Locate every blood parasite and identify its species.
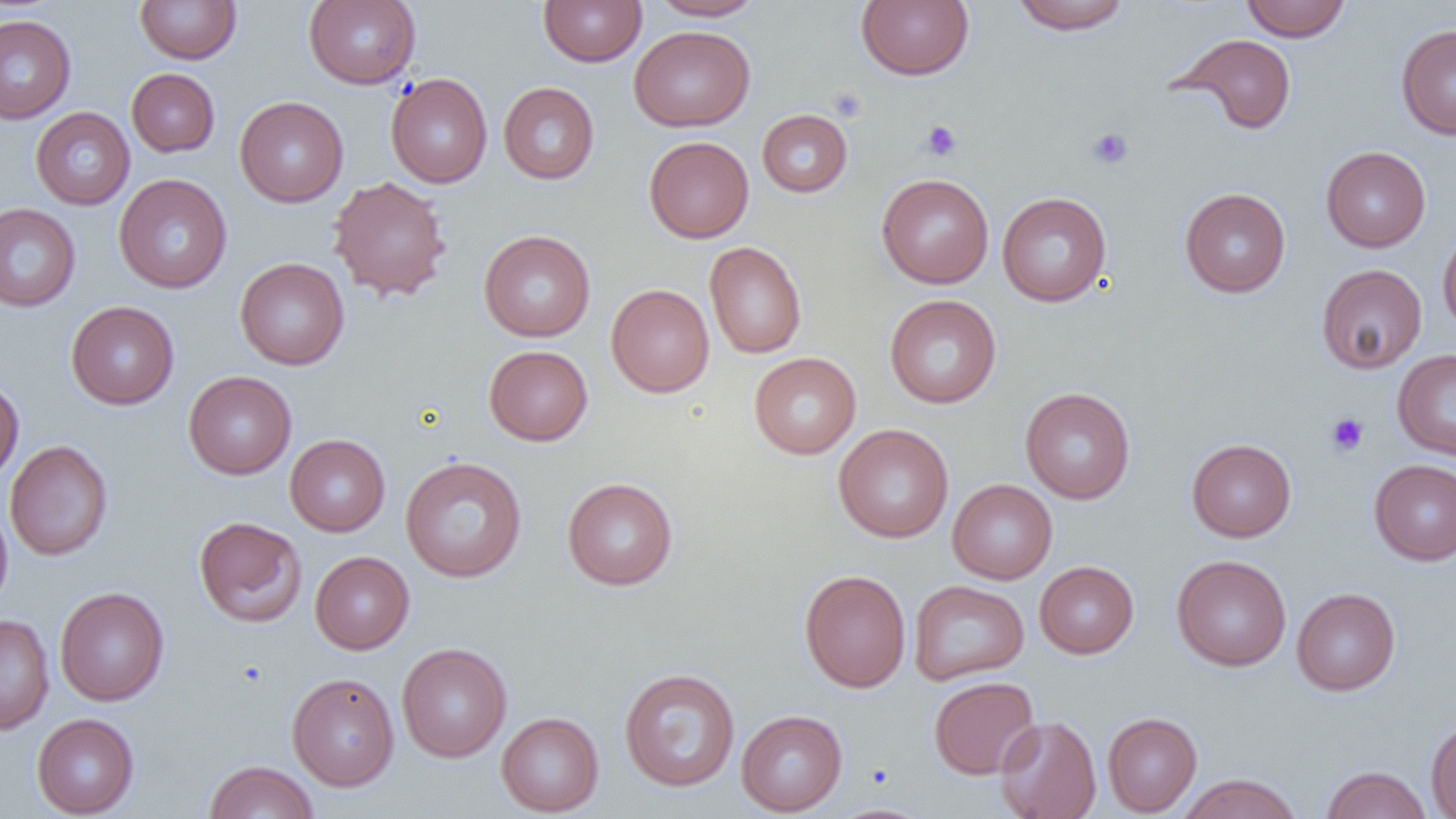
No blood parasites observed.

Approximate bounding boxes as (x1,y1)-(x2,y2) corner pairs in pixels. Uninfected red blood cell locations: (135,0)-(241,64), (304,0)-(421,89), (538,0)-(647,67), (650,0)-(765,21), (856,0)-(974,81), (1010,0)-(1131,35), (1241,0)-(1351,42), (0,14)-(76,123), (1396,24)-(1456,140), (629,26)-(755,131), (1171,32)-(1298,135), (126,68)-(220,157), (386,73)-(493,188), (498,82)-(600,184), (234,96)-(348,207), (30,107)-(135,210), (757,108)-(853,198), (643,136)-(754,243), (1321,146)-(1431,252), (877,173)-(994,289), (114,174)-(231,294), (327,176)-(453,302), (1180,187)-(1291,297), (997,192)-(1111,307), (0,203)-(81,312), (1437,224)-(1456,339), (479,229)-(596,342), (705,242)-(806,359), (235,257)-(349,370), (1316,264)-(1427,374), (606,284)-(715,397), (884,295)-(1001,409), (66,301)-(179,409), (483,345)-(593,446), (1392,349)-(1456,460), (749,352)-(862,459), (183,370)-(297,479), (0,377)-(24,484), (1020,387)-(1135,504), (833,424)-(954,543), (285,434)-(390,536), (1186,438)-(1296,542), (5,440)-(113,561), (400,456)-(527,582), (1369,459)-(1456,565), (562,477)-(678,590), (947,479)-(1057,584), (0,498)-(13,613), (194,516)-(307,627), (310,551)-(414,654), (1171,555)-(1291,671), (1035,561)-(1139,658), (799,569)-(911,692), (908,579)-(1029,685), (55,586)-(169,706), (1291,587)-(1401,696), (0,613)-(54,735), (396,642)-(512,762), (618,667)-(741,792), (286,672)-(400,790), (928,676)-(1040,780), (736,710)-(847,816), (496,712)-(604,816), (1102,712)-(1202,816), (31,713)-(139,818), (995,715)-(1101,819), (1425,716)-(1456,818), (204,760)-(320,818), (1320,765)-(1432,819), (1174,773)-(1304,819), (824,803)-(937,819). Platelet locations: (827,86)-(867,122), (920,120)-(962,161), (1086,127)-(1134,170), (1326,413)-(1369,456). Slide-level diagnosis: negative for blood parasites. Single field of view. Light microscopy. 1000x magnification. Image is 1456×819 pixels. Thin blood film.